Draw a bounding box around every malaria parasite.
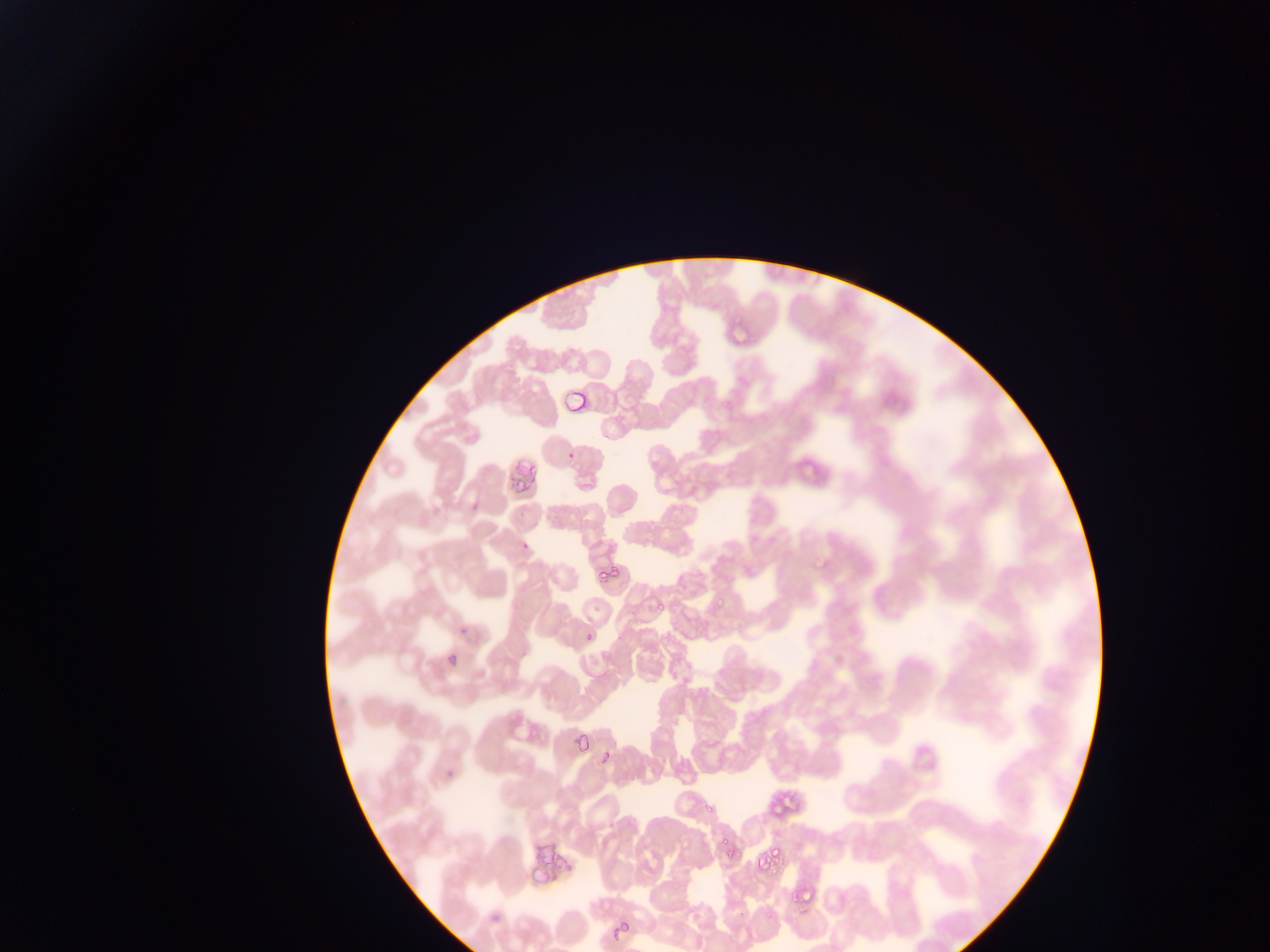

Approximate bounding boxes as left top right bottom in pixels.
Malaria parasites: 564 440 585 465; 596 560 618 583; 647 593 668 615; 713 594 730 609; 579 621 606 646; 531 717 550 746; 573 736 589 754; 600 750 612 763; 701 800 718 817; 719 837 730 848; 716 849 731 866; 758 853 777 879; 788 881 806 907; 620 911 634 924.

One field of view. Thin blood film. Collected in Ghana. Image is 1270×952 pixels. Photographed through a microscope with a mobile-phone camera.